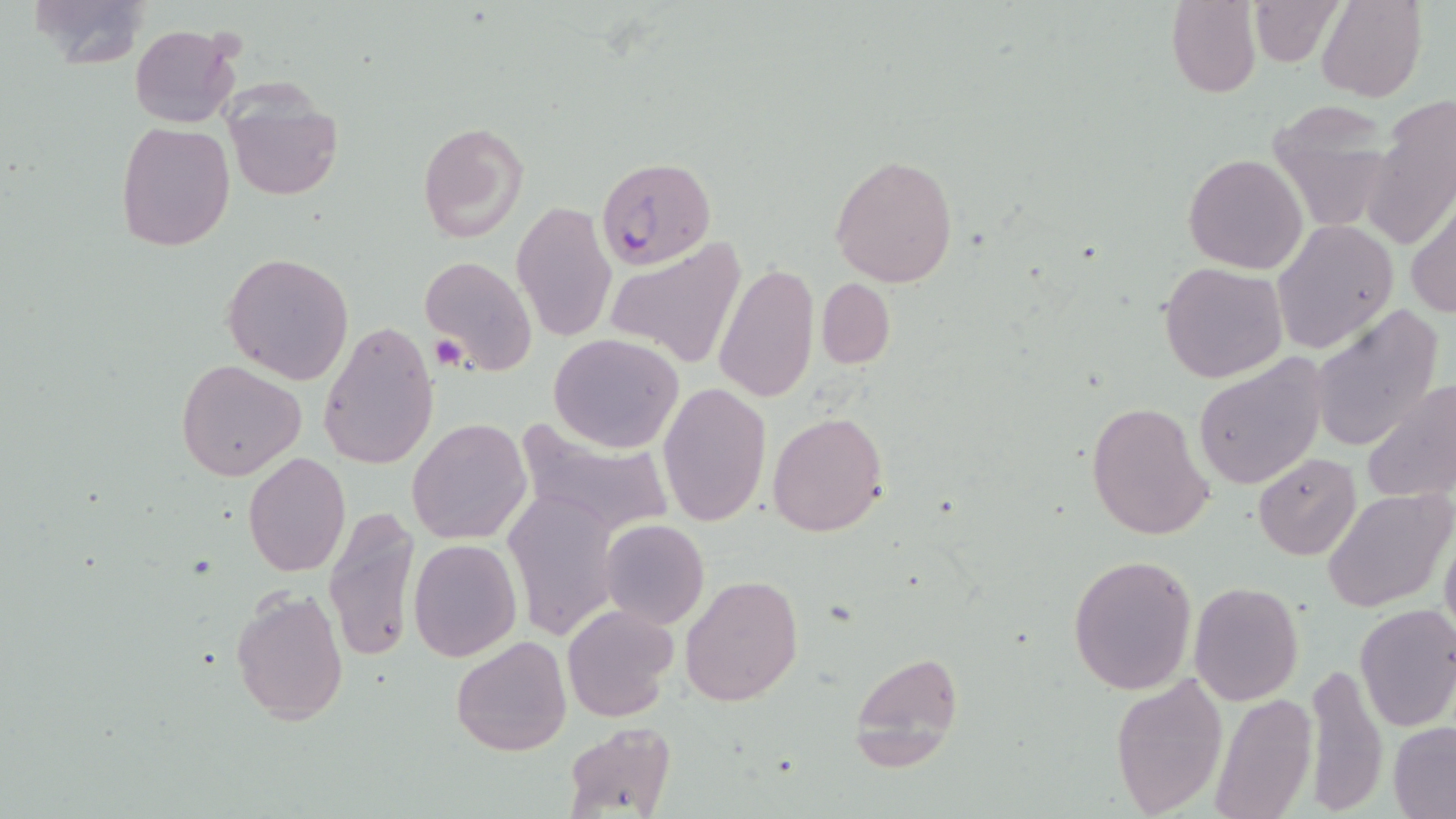 Approximate bounding boxes as (x1,y1)-(x2,y2) corner pairs in pixels. Plasmodium falciparum-infected red blood cell locations: (595,157)-(715,271). Uninfected red blood cell locations: (24,0)-(151,70), (1249,0)-(1344,67), (1166,1)-(1261,97), (1315,1)-(1426,102), (131,25)-(240,128), (1369,95)-(1455,248), (225,96)-(343,203), (1265,102)-(1397,231), (418,120)-(530,245), (115,122)-(234,250), (829,153)-(959,289), (1183,153)-(1309,274), (1407,199)-(1456,319), (512,201)-(618,343), (1273,220)-(1399,354), (606,241)-(748,370), (222,251)-(354,384), (419,254)-(538,376), (1159,261)-(1288,385), (712,262)-(819,404), (816,277)-(896,368), (1309,307)-(1444,454), (317,320)-(438,472), (548,334)-(684,454), (1190,353)-(1330,491), (176,359)-(308,481), (1360,379)-(1456,507), (658,382)-(771,526), (1087,400)-(1214,542), (767,411)-(890,536), (406,416)-(531,546), (511,420)-(676,539), (1252,452)-(1362,560), (244,453)-(349,576), (1325,488)-(1453,611), (502,490)-(623,640), (323,506)-(422,664), (599,519)-(710,630), (1439,527)-(1456,645), (408,540)-(521,661), (1066,552)-(1198,696), (681,572)-(803,706), (1189,581)-(1303,703), (229,586)-(349,727), (1354,604)-(1456,732), (559,605)-(679,723), (451,635)-(572,758), (850,648)-(963,767), (1302,662)-(1387,810), (1111,672)-(1228,818), (1212,692)-(1315,819), (1388,722)-(1456,817), (564,723)-(676,818). Platelet locations: (430,335)-(468,370). Slide-level diagnosis: Plasmodium falciparum. 1000x magnification. Thin blood film. May-Grünwald-Giemsa-stained preparation. One field of a larger specimen. Optical microscopy. Image is 1456×819 pixels.